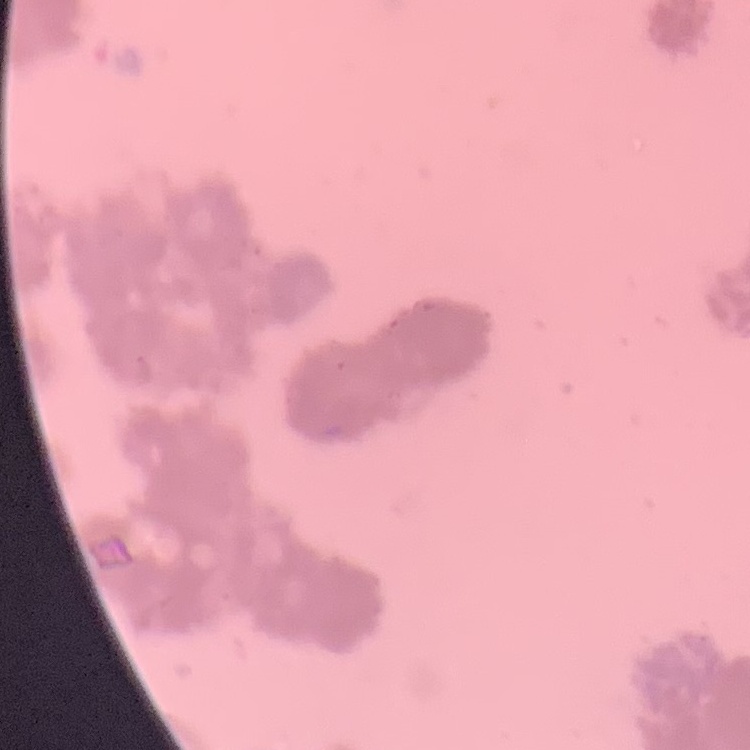 The red blood cells show rouleaux formation. Square crop of a larger photomicrograph. Thin blood smear. Stained with either Field's or Giemsa.